Report the malaria status of this cell.
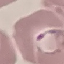
It is parasitized.

Summary:
  - Capture: smartphone through the microscope eyepiece
  - Image type: cell patch, automatically extracted from a larger field of view and resized to 64 × 64 pixels
  - Stain: Giemsa
  - Preparation: thin smear